Name the cell type shown.
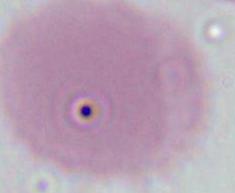

This is an erythrocyte.

Summary:
  - Modality: micrograph
  - Magnification: 1000x